Report the malaria status of this cell.
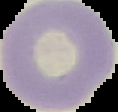
It is uninfected.

Summary:
  - Preparation: thin blood smear
  - Image type: segmented cell region with the area outside set to black
  - Image size: 118×112 pixels